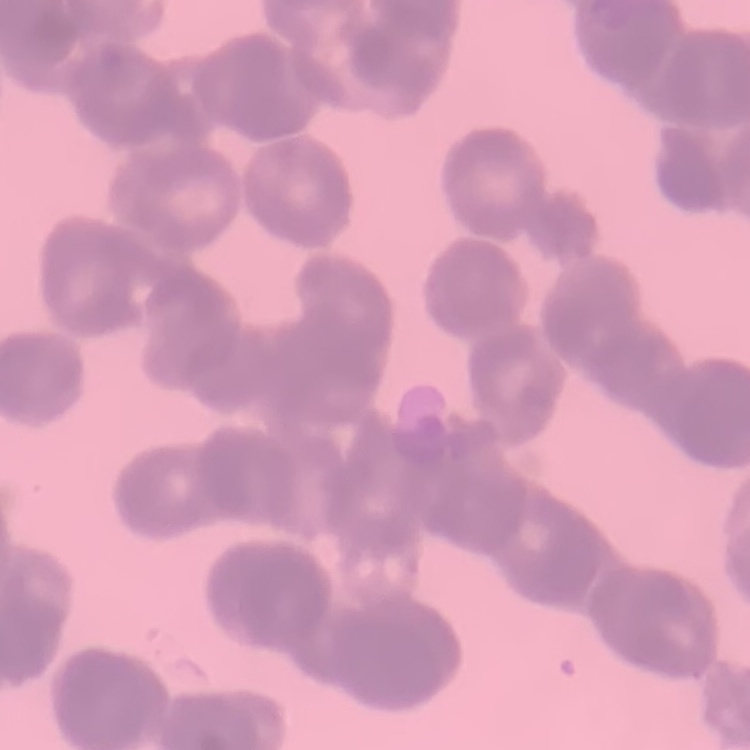

The red blood cells exhibit rouleaux formation. Stained with either Field's or Giemsa. One tile cut from a larger photomicrograph. Thin blood film.